Report the malaria status of this cell.
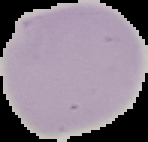
It is uninfected.

Image is 148×142 pixels. From a thin blood film. Cell region segmented out of the field of view; the surrounding area is masked to black.